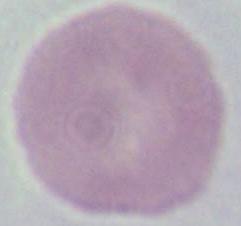
modality = photomicrograph
magnification = 1000x
identification = erythrocyte